Report the malaria status of this cell.
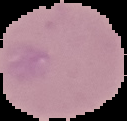

It is uninfected.

Summary:
  - Image size: 127×121 pixels
  - Image type: cell region segmented out of the field of view; surrounding area masked to black
  - Preparation: thin blood smear